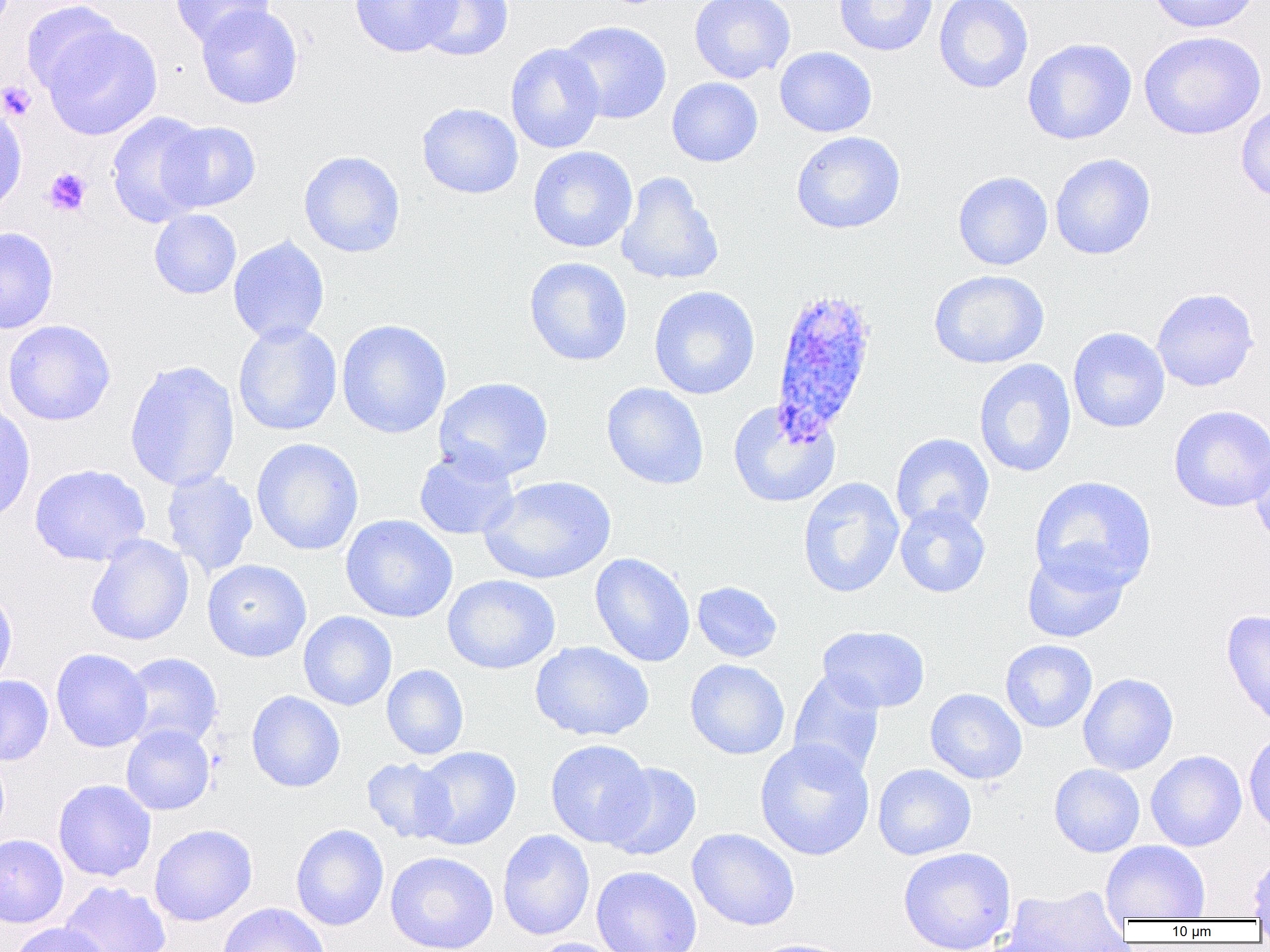
{
  "slide_level_diagnosis": "Plasmodium ovale",
  "modality": "light microscopy",
  "plasmodium_ovale_infected_red_blood_cell_locations": "approximate bounding boxes as (x1, y1, x2, y2) in pixels: (769, 285, 879, 443)",
  "field_of_view": "one of a larger specimen",
  "uninfected_red_blood_cell_locations": "approximate bounding boxes as (x1, y1, x2, y2) in pixels: (169, 0, 275, 47), (349, 0, 460, 57), (413, 0, 514, 62), (689, 0, 796, 84), (833, 0, 938, 56), (933, 0, 1034, 93), (1146, 0, 1262, 33), (20, 1, 126, 98), (196, 4, 303, 109), (41, 20, 162, 140), (558, 21, 673, 124), (1138, 30, 1267, 140), (1022, 38, 1137, 145), (505, 42, 605, 154), (774, 46, 877, 137), (667, 77, 763, 167), (0, 100, 28, 217), (416, 102, 524, 199), (1236, 102, 1270, 205), (106, 111, 212, 228), (158, 120, 261, 213), (790, 130, 906, 234), (527, 146, 638, 252), (298, 151, 405, 258), (1050, 153, 1156, 260), (616, 171, 724, 286), (952, 171, 1053, 271), (149, 209, 242, 299), (0, 227, 59, 334), (228, 235, 330, 346), (524, 257, 632, 367), (928, 269, 1049, 369), (648, 286, 760, 400), (1151, 288, 1259, 392), (336, 319, 452, 439), (1, 320, 115, 426), (233, 321, 342, 436), (1068, 327, 1170, 433), (973, 358, 1077, 478), (124, 359, 240, 492), (433, 377, 554, 482), (601, 383, 709, 490), (0, 398, 36, 524), (728, 400, 841, 508), (1168, 405, 1270, 512), (891, 433, 995, 533), (251, 438, 364, 555), (1247, 441, 1270, 548), (413, 447, 520, 540), (29, 464, 150, 566), (161, 470, 258, 578), (479, 475, 616, 585), (1029, 475, 1158, 593), (797, 477, 904, 598), (894, 503, 991, 598), (340, 514, 458, 623), (85, 535, 194, 646), (1021, 547, 1129, 643), (590, 553, 695, 667), (202, 559, 312, 662), (442, 574, 561, 675), (692, 581, 783, 662), (0, 586, 18, 690), (1221, 609, 1270, 728), (298, 611, 397, 711), (817, 625, 930, 713), (1000, 639, 1097, 732), (530, 641, 654, 742), (51, 648, 152, 752), (120, 652, 223, 751), (685, 659, 790, 760), (381, 664, 469, 760), (788, 669, 885, 780), (1078, 673, 1178, 775), (0, 675, 54, 766), (925, 688, 1027, 784), (246, 690, 345, 792), (121, 724, 215, 815), (1244, 731, 1270, 837), (754, 738, 875, 861), (545, 739, 654, 847), (413, 746, 521, 849), (1146, 750, 1247, 852), (361, 757, 456, 844), (600, 762, 702, 861), (872, 763, 976, 860), (1049, 764, 1145, 857), (52, 779, 156, 882), (149, 824, 257, 926), (290, 824, 389, 931), (687, 828, 800, 931), (497, 829, 595, 940), (0, 834, 69, 928), (1100, 840, 1211, 922), (897, 846, 1017, 952), (1248, 850, 1270, 920), (385, 851, 499, 952), (591, 866, 703, 952), (60, 881, 171, 952), (998, 884, 1130, 951), (216, 902, 331, 952), (10, 922, 111, 952), (528, 938, 630, 952), (745, 938, 855, 952)",
  "platelet_locations": "approximate bounding boxes as (x1, y1, x2, y2) in pixels: (0, 81, 37, 121), (44, 167, 92, 216)",
  "image_size": "1270×952 pixels",
  "preparation": "thin blood film",
  "magnification": "1000x"
}